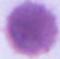

modality = micrograph
identification = erythrocyte
magnification = 1000x